Point out every malaria parasite and every leukocyte.
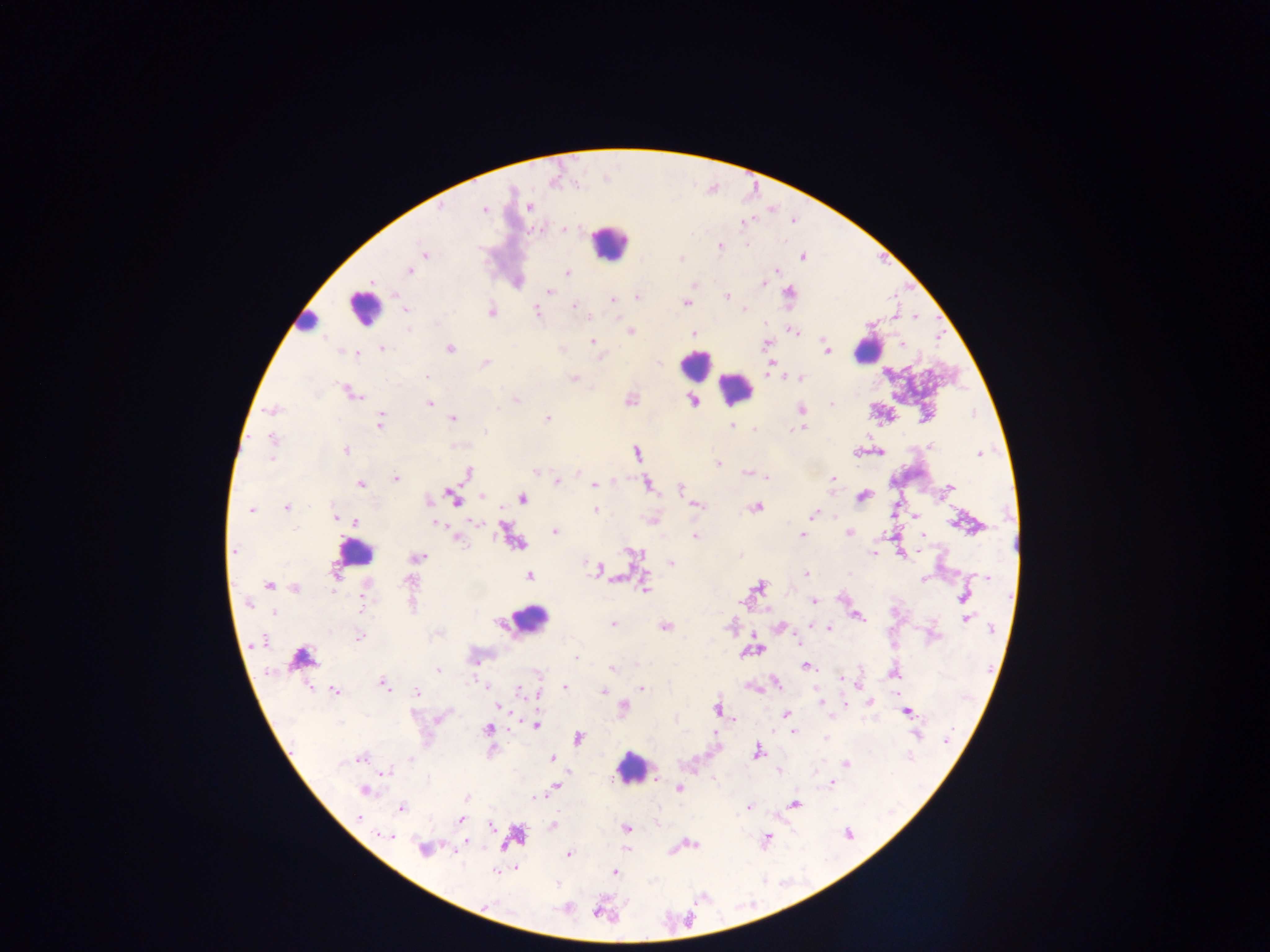
Approximate centers as (x, y) in pixels.
Malaria parasites: (441, 207), (529, 207), (484, 208), (743, 224), (564, 228), (746, 245), (720, 246), (425, 254), (803, 256), (681, 258), (410, 270), (776, 271), (567, 273), (371, 282), (763, 283), (695, 284), (548, 292), (789, 294), (638, 297), (727, 297), (612, 300), (686, 303), (574, 304), (404, 309), (744, 309), (491, 312), (537, 312), (590, 316), (407, 330), (631, 331), (794, 332), (693, 334), (592, 342), (766, 344), (825, 344), (902, 344), (382, 349), (450, 349), (562, 349), (827, 349), (342, 351), (356, 353), (600, 357), (485, 363), (426, 377), (573, 379), (800, 379), (353, 394), (515, 400), (630, 401), (694, 402), (429, 403), (832, 404), (800, 409), (271, 410), (453, 418), (546, 418), (381, 421), (732, 426), (799, 428), (755, 429), (486, 431), (272, 440), (930, 446), (346, 450), (636, 453), (979, 453), (718, 464), (535, 471), (468, 472), (746, 473), (767, 477), (396, 478), (833, 478), (556, 481), (360, 485), (594, 485), (647, 485), (681, 487), (950, 487), (482, 496), (862, 496), (452, 498), (522, 499), (696, 506), (286, 507), (756, 507), (251, 509), (596, 510), (813, 514), (916, 516), (336, 518), (355, 522), (435, 523), (477, 523), (555, 531), (849, 532), (803, 535), (922, 535), (695, 537), (457, 538), (235, 550), (633, 553), (874, 553), (741, 555), (902, 555), (418, 557), (672, 563), (587, 564), (598, 568), (806, 573), (849, 573), (528, 576), (986, 578), (923, 579), (408, 582), (268, 585), (759, 586), (645, 587), (294, 588), (964, 596), (362, 598), (813, 601), (249, 605), (964, 608), (361, 610), (272, 612), (858, 617), (966, 619), (613, 623), (665, 627), (828, 628), (991, 630), (359, 637), (261, 641), (798, 642), (575, 657), (807, 666), (612, 668), (861, 668), (438, 670), (895, 673), (842, 679), (473, 680), (775, 683), (384, 685), (565, 687), (642, 688), (488, 689), (334, 690), (520, 691), (603, 691), (417, 692), (537, 695), (820, 701), (871, 702), (846, 704), (501, 707), (624, 707), (716, 709), (908, 712), (786, 714), (734, 719), (536, 724), (487, 729), (794, 732), (918, 735), (578, 738), (825, 738), (947, 739), (491, 752), (757, 752), (908, 756), (360, 757), (410, 759), (552, 759), (343, 762), (845, 763), (385, 772), (778, 772), (655, 778), (831, 783), (555, 787), (679, 789), (364, 791), (466, 798), (538, 798), (795, 804), (749, 807), (401, 808), (358, 817), (460, 820), (491, 825), (553, 825), (626, 828), (848, 834), (387, 836), (766, 840), (692, 843), (424, 850), (568, 854), (496, 872), (614, 872), (487, 906).
Leukocytes: (608, 241), (364, 308), (306, 321), (867, 349), (695, 366), (735, 389), (355, 552), (528, 620), (304, 658), (633, 768).

field of view = single
preparation = thick blood smear
capture = mobile-phone photograph through a microscope
country = Ghana
image size = 1270×952 pixels